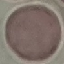

Malaria status: uninfected. Cell patch, automatically extracted from a larger field of view and resized to 64 × 64 pixels. Acquired by smartphone through the microscope eyepiece. Thin blood smear. Giemsa stain.